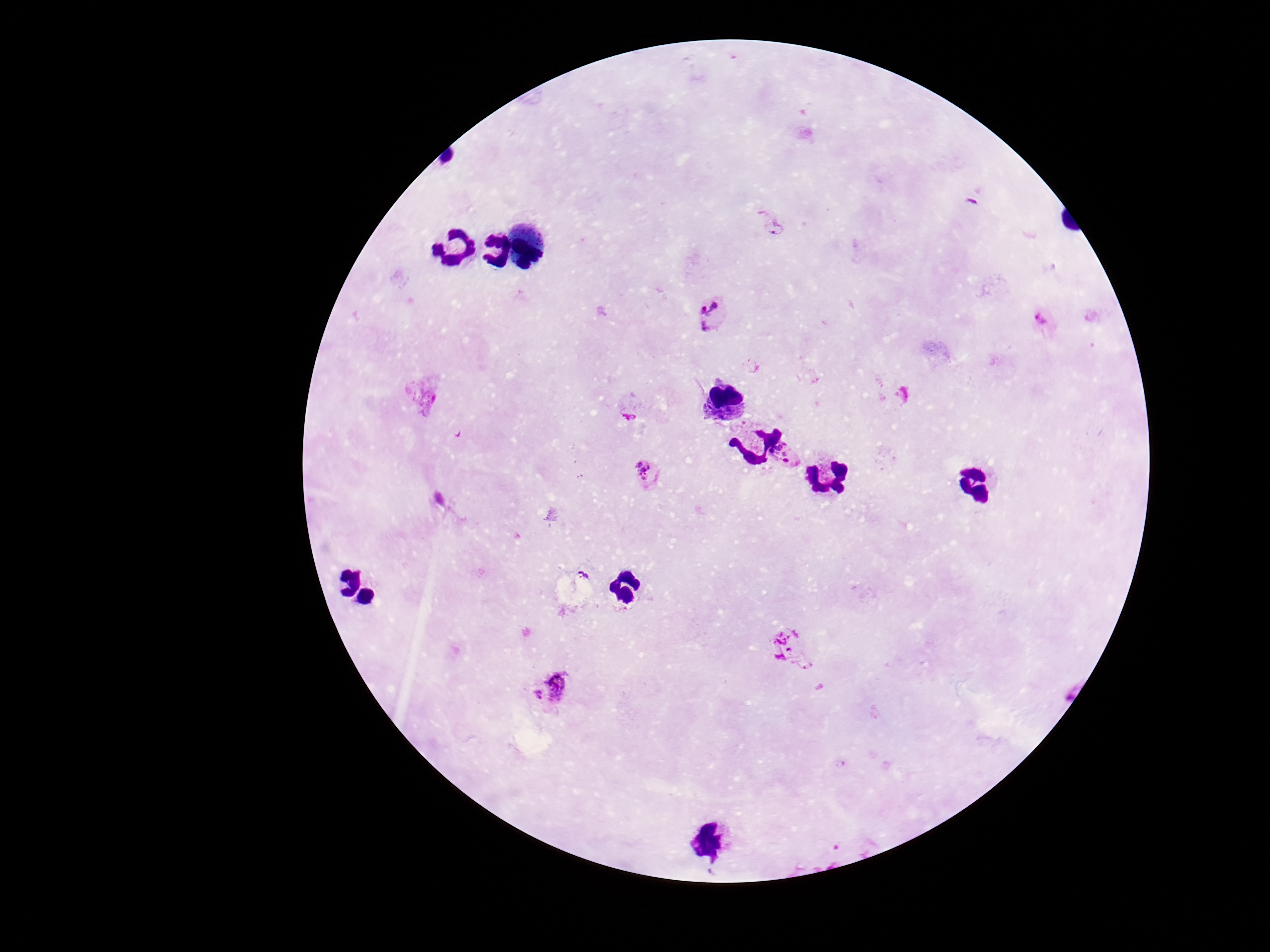
capture = smartphone camera through the microscope eyepiece
preparation = thick blood smear
stain = Giemsa
magnification = 100x
patient malaria status = infected
image size = 1270×952 pixels
Plasmodium parasite locations = approximate centers as [x, y] in pixels: [775, 225], [714, 315], [1044, 320], [423, 392], [632, 406], [786, 454], [650, 474], [792, 650], [562, 684], [534, 696]
field of view = one from this slide